Classify this cell by malaria status.
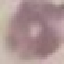

It is uninfected.

capture = smartphone camera at the microscope eyepiece
stain = Giemsa
preparation = thin blood smear
image type = cell patch, automatically extracted from a larger field of view and resized to 64 × 64 pixels